Classify this cell by malaria status.
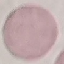
Uninfected.

{
  "capture": "smartphone camera at the microscope eyepiece",
  "image_type": "cell patch, automatically extracted from a larger field of view and resized to 64 × 64 pixels",
  "stain": "Giemsa",
  "preparation": "thin blood film"
}